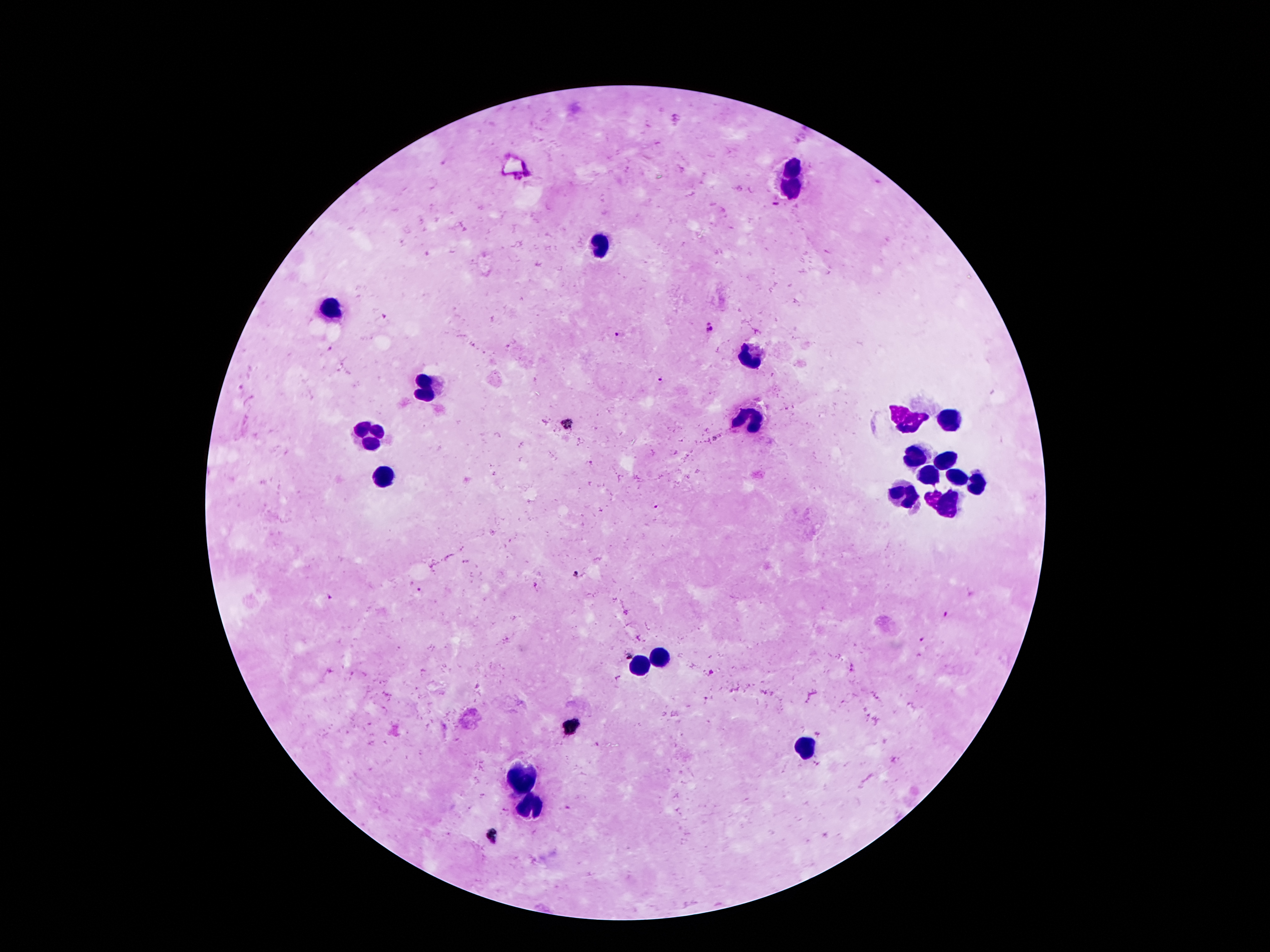

Approximate object centers, in pixels from the top-left corner. Plasmodium parasite locations: (x=709, y=328), (x=617, y=333), (x=661, y=379), (x=568, y=424), (x=575, y=575), (x=418, y=591), (x=330, y=597), (x=921, y=640), (x=626, y=653). Leukocyte locations: (x=790, y=169), (x=791, y=188), (x=603, y=246), (x=331, y=310), (x=749, y=357), (x=425, y=389), (x=904, y=418), (x=748, y=419), (x=949, y=423), (x=371, y=437), (x=917, y=458), (x=944, y=461), (x=384, y=474), (x=932, y=475), (x=955, y=477), (x=978, y=484), (x=906, y=494), (x=945, y=502), (x=664, y=654), (x=642, y=667), (x=805, y=748), (x=519, y=780), (x=531, y=806). One field from this slide. Image is 1270×952 pixels. Giemsa-stained preparation. Patient malaria status: infected with Plasmodium falciparum. Photographed through the microscope eyepiece with a smartphone camera. 100x magnification. Thick blood film.